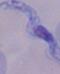

magnification = 1000x
modality = micrograph
identification = trypanosome